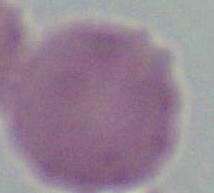

Summary:
  - Identification: red blood cell
  - Magnification: 1000x
  - Modality: photomicrograph